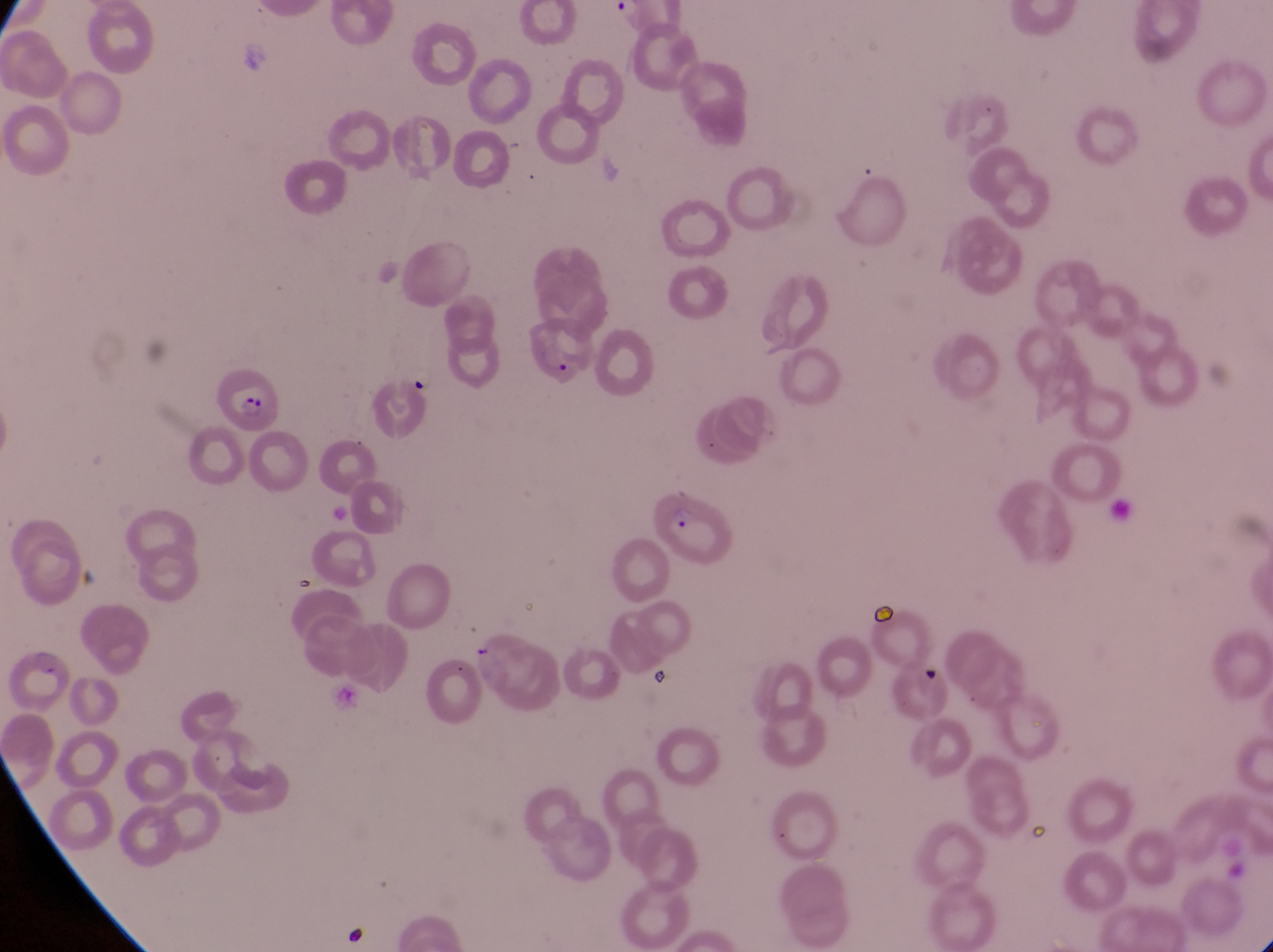
Approximate bounding boxes as [left, top, right, bottom] in pixels.
Summary:
  - Parasitised red blood cell locations: [522, 318, 599, 398], [209, 364, 281, 436], [646, 484, 745, 579]
  - Trophozoite locations: [409, 360, 442, 399]
  - Artifact (platelet-like body, stain precipitate, or debris) locations: [868, 587, 907, 622], [921, 664, 948, 694]
  - Preparation: thin blood smear
  - Capture: smartphone photograph through the eyepiece of an Olympus CX-23 microscope
  - Magnification: 1000x
  - Country: Uganda
  - Image size: 1273×952 pixels
  - Field of view: single